Point out each malaria parasite.
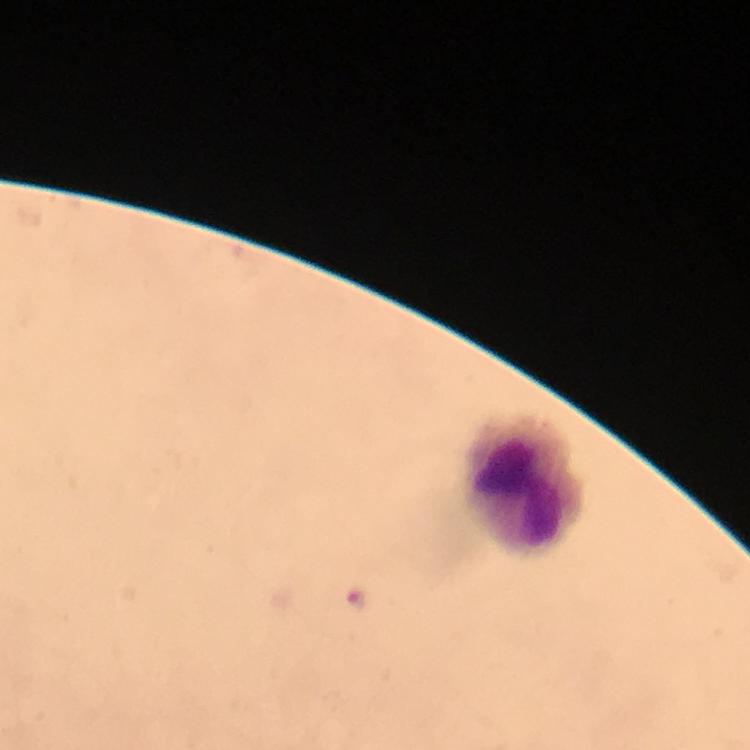

Approximate centers as {x, y} in pixels.
Malaria parasites: {358, 603}.

stain = Giemsa
context = from a malaria diagnostic workup
leukocyte locations = approximate centers as {x, y} in pixels: {529, 486}
capture = smartphone camera through the microscope
preparation = thick blood film
cropped from = a single field of view
image size = 750×750 pixels
immersion oil = applied
magnification = 100x